Report the malaria status of this cell.
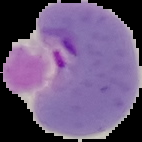
Parasitized.

Image is 142×142 pixels. The area outside the segmented cell region is set to black. From a thin blood film.